Assess this cell for malaria.
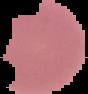

Parasitized.

{
  "image_type": "segmented cell region with the area outside set to black",
  "image_size": "88×94 pixels",
  "preparation": "thin blood film"
}